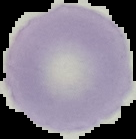

Summary:
  - Result: negative for malaria parasites
  - Preparation: thin blood film
  - Image type: cell region segmented out of the field of view; surrounding area masked to black
  - Image size: 136×139 pixels